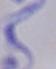

Summary:
  - Identification: trypanosome
  - Modality: photomicrograph
  - Magnification: 1000x